State the blood parasite species.
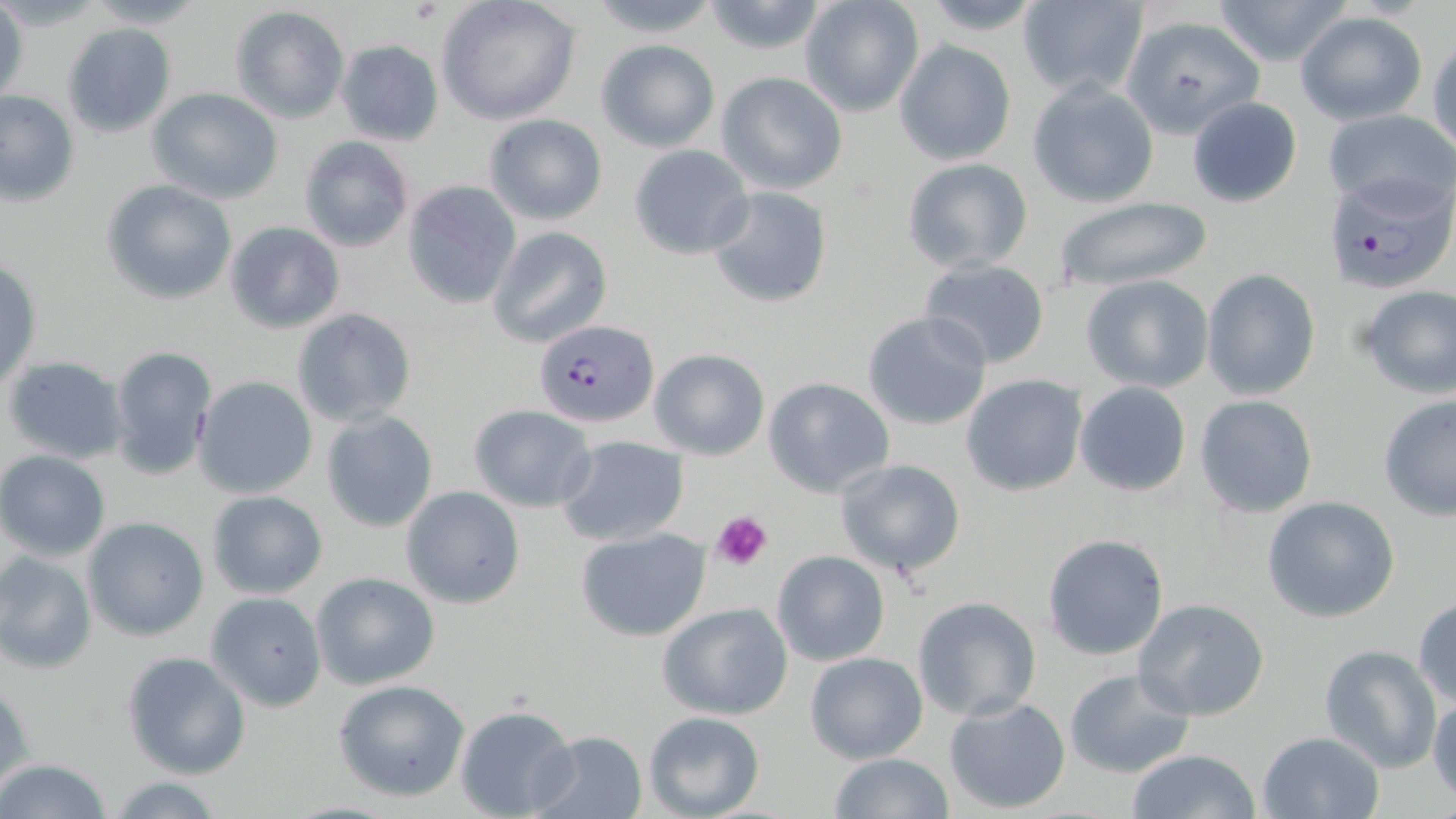
Plasmodium falciparum.

preparation = thin blood smear
Plasmodium falciparum-infected red blood cell locations = approximate bounding boxes as named x1/y1/x2/y2 corners in pixels: (x1=1322, y1=175, x2=1455, y2=297), (x1=535, y1=318, x2=656, y2=425)
image size = 1456×819 pixels
stain = May-Grünwald-Giemsa
field of view = one of a larger specimen
platelet locations = approximate bounding boxes as named x1/y1/x2/y2 corners in pixels: (x1=407, y1=1, x2=441, y2=25), (x1=711, y1=510, x2=773, y2=572)
uninfected red blood cell locations = approximate bounding boxes as named x1/y1/x2/y2 corners in pixels: (x1=80, y1=0, x2=209, y2=28), (x1=435, y1=0, x2=582, y2=126), (x1=583, y1=0, x2=723, y2=37), (x1=798, y1=0, x2=925, y2=118), (x1=1016, y1=0, x2=1150, y2=100), (x1=1210, y1=0, x2=1352, y2=69), (x1=699, y1=2, x2=830, y2=55), (x1=1, y1=4, x2=29, y2=108), (x1=229, y1=6, x2=350, y2=123), (x1=1295, y1=11, x2=1428, y2=124), (x1=1120, y1=14, x2=1265, y2=139), (x1=61, y1=23, x2=176, y2=138), (x1=1428, y1=31, x2=1456, y2=158), (x1=594, y1=38, x2=720, y2=152), (x1=335, y1=39, x2=443, y2=146), (x1=893, y1=39, x2=1017, y2=166), (x1=717, y1=72, x2=847, y2=196), (x1=1027, y1=79, x2=1161, y2=209), (x1=146, y1=87, x2=285, y2=204), (x1=0, y1=90, x2=78, y2=207), (x1=1187, y1=96, x2=1303, y2=207), (x1=1322, y1=109, x2=1456, y2=217), (x1=482, y1=113, x2=608, y2=225), (x1=298, y1=136, x2=415, y2=252), (x1=627, y1=144, x2=755, y2=259), (x1=901, y1=158, x2=1034, y2=274), (x1=102, y1=180, x2=236, y2=304), (x1=402, y1=181, x2=520, y2=310), (x1=705, y1=186, x2=835, y2=308), (x1=1049, y1=194, x2=1216, y2=293), (x1=223, y1=221, x2=345, y2=334), (x1=487, y1=226, x2=613, y2=349), (x1=239, y1=245, x2=373, y2=388), (x1=917, y1=257, x2=1051, y2=371), (x1=1, y1=260, x2=41, y2=389), (x1=1202, y1=268, x2=1321, y2=402), (x1=1080, y1=275, x2=1213, y2=393), (x1=1355, y1=284, x2=1456, y2=400), (x1=290, y1=308, x2=417, y2=428), (x1=862, y1=312, x2=993, y2=431), (x1=107, y1=344, x2=217, y2=478), (x1=648, y1=348, x2=771, y2=460), (x1=4, y1=355, x2=128, y2=463), (x1=960, y1=374, x2=1089, y2=497), (x1=192, y1=375, x2=318, y2=501), (x1=762, y1=377, x2=895, y2=498), (x1=1074, y1=380, x2=1193, y2=498), (x1=1194, y1=394, x2=1321, y2=519), (x1=1377, y1=394, x2=1456, y2=521), (x1=468, y1=405, x2=597, y2=513), (x1=321, y1=411, x2=438, y2=533), (x1=555, y1=435, x2=691, y2=547), (x1=0, y1=450, x2=111, y2=561), (x1=834, y1=458, x2=966, y2=578), (x1=400, y1=485, x2=525, y2=609), (x1=206, y1=489, x2=328, y2=599), (x1=1262, y1=494, x2=1401, y2=624), (x1=82, y1=517, x2=209, y2=642), (x1=575, y1=528, x2=712, y2=642), (x1=1042, y1=533, x2=1169, y2=660), (x1=771, y1=549, x2=891, y2=665), (x1=0, y1=551, x2=96, y2=673), (x1=311, y1=571, x2=440, y2=690), (x1=206, y1=593, x2=326, y2=711), (x1=1411, y1=595, x2=1456, y2=707), (x1=911, y1=596, x2=1042, y2=721), (x1=1131, y1=598, x2=1272, y2=722), (x1=655, y1=601, x2=794, y2=721), (x1=1316, y1=645, x2=1442, y2=773), (x1=121, y1=651, x2=251, y2=779), (x1=804, y1=651, x2=929, y2=764), (x1=1063, y1=667, x2=1195, y2=778), (x1=334, y1=679, x2=470, y2=802), (x1=1, y1=684, x2=34, y2=796), (x1=1428, y1=692, x2=1456, y2=802), (x1=943, y1=695, x2=1073, y2=812), (x1=453, y1=704, x2=578, y2=817), (x1=643, y1=711, x2=765, y2=819), (x1=529, y1=730, x2=648, y2=819), (x1=1257, y1=731, x2=1385, y2=818), (x1=1124, y1=748, x2=1262, y2=819), (x1=827, y1=752, x2=953, y2=819), (x1=0, y1=758, x2=111, y2=819), (x1=107, y1=776, x2=225, y2=817)
magnification = 1000x
modality = optical microscopy